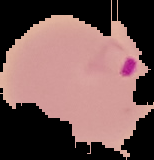

{
  "result": "Plasmodium parasites detected",
  "image_size": "154×160 pixels",
  "image_type": "segmented cell region on a black background",
  "preparation": "thin blood smear"
}